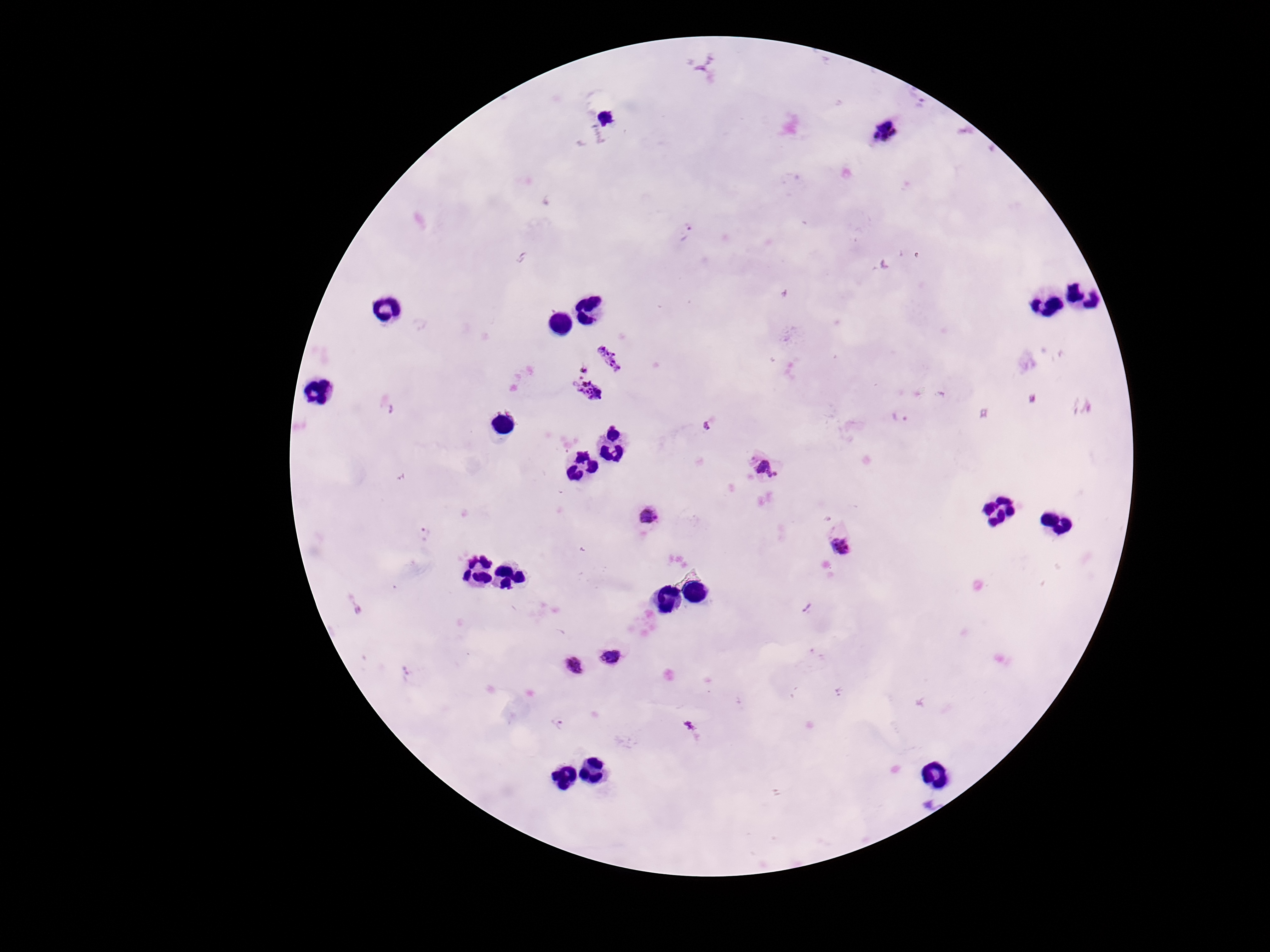

Approximate centers as [x, y] in pixels.
Summary:
  - Plasmodium parasite locations: [882, 131], [685, 233], [611, 357], [584, 369], [586, 394], [900, 416], [767, 469], [649, 517], [425, 532], [840, 547], [354, 607], [808, 608], [611, 657], [574, 666], [405, 673], [560, 725], [690, 726]
  - Field of view: one from this slide
  - Image size: 1270×952 pixels
  - Magnification: 100x
  - Preparation: thick blood smear
  - Patient malaria status: positive
  - Capture: smartphone camera through the microscope eyepiece
  - Stain: Giemsa